Locate every Plasmodium parasite.
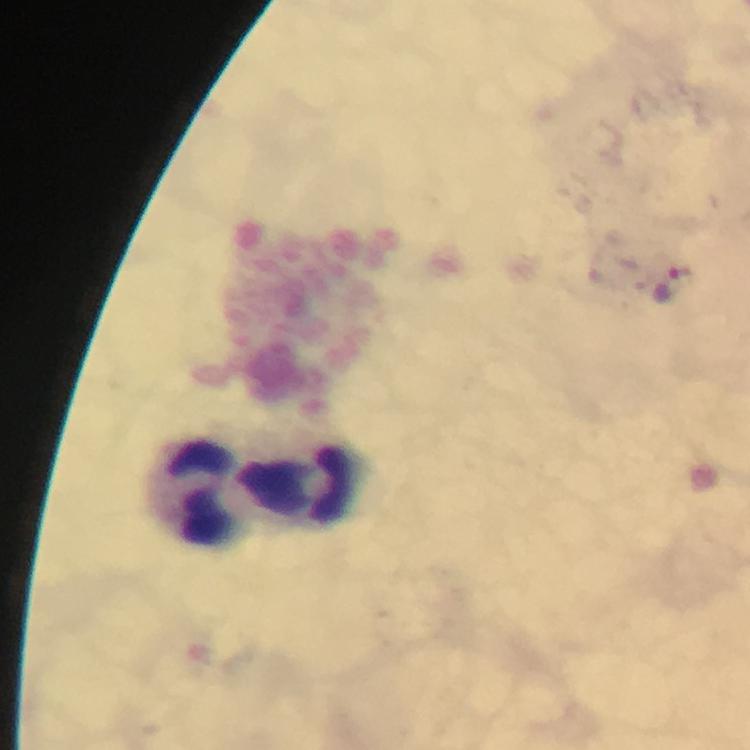
Approximate centers as {x, y} in pixels.
Plasmodium parasites: {670, 286}.

Leukocyte locations: {302, 484}, {199, 488}. Smartphone photograph taken through a microscope. Cropped region of a single field of view. Thick blood smear. 100x magnification. From a diagnostic examination for malaria. Image is 750×750 pixels. Giemsa-stained preparation. Immersion oil was used.